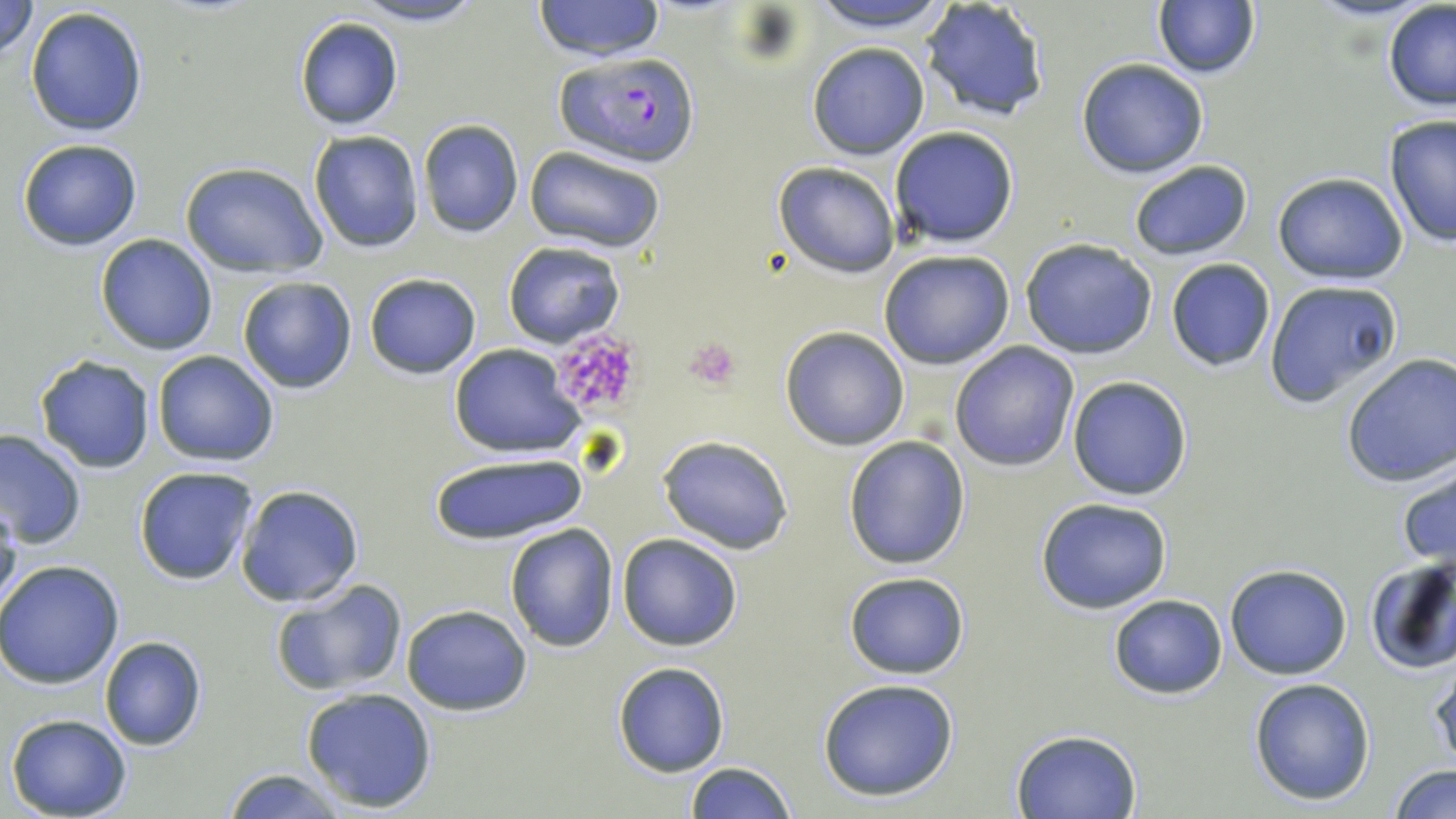

Approximate bounding boxes as [x1, y1, x2, y2] in pixels. Plasmodium falciparum-infected red blood cell locations: [557, 50, 698, 168]. Uninfected red blood cell locations: [0, 0, 38, 61], [351, 0, 489, 27], [532, 0, 663, 61], [805, 0, 953, 34], [1301, 0, 1438, 22], [920, 1, 1050, 123], [1151, 1, 1261, 81], [1382, 4, 1456, 112], [26, 5, 149, 138], [292, 17, 405, 131], [807, 41, 931, 159], [1075, 58, 1209, 178], [1383, 114, 1455, 248], [417, 119, 524, 237], [889, 126, 1020, 248], [308, 130, 424, 253], [16, 137, 144, 251], [525, 147, 667, 255], [1127, 159, 1252, 262], [178, 161, 329, 278], [772, 161, 902, 277], [1271, 171, 1409, 285], [95, 234, 217, 355], [1019, 237, 1159, 360], [503, 241, 626, 349], [879, 251, 1017, 371], [1165, 258, 1276, 372], [363, 273, 483, 379], [236, 275, 358, 394], [1263, 278, 1403, 407], [779, 327, 909, 449], [949, 341, 1080, 470], [449, 345, 588, 456], [151, 349, 279, 465], [1338, 352, 1456, 487], [34, 356, 156, 473], [1067, 375, 1193, 500], [0, 430, 87, 550], [658, 435, 795, 553], [843, 436, 971, 570], [428, 449, 590, 546], [1396, 459, 1456, 570], [134, 467, 258, 584], [236, 485, 363, 607], [1035, 497, 1173, 614], [0, 500, 23, 617], [504, 524, 618, 652], [616, 532, 744, 651], [1364, 555, 1456, 675], [0, 560, 125, 688], [1224, 565, 1352, 680], [843, 570, 971, 678], [270, 578, 409, 698], [1108, 594, 1227, 700], [401, 604, 532, 715], [99, 636, 206, 751], [1429, 660, 1456, 772], [612, 662, 730, 777], [1248, 677, 1377, 805], [817, 678, 960, 802], [299, 686, 440, 813], [5, 713, 132, 819], [1011, 728, 1141, 817], [683, 761, 795, 818], [1388, 765, 1455, 819], [221, 768, 350, 819]. Platelet locations: [549, 328, 645, 418], [685, 339, 741, 390]. Slide-level diagnosis: Plasmodium falciparum. Image is 1456×819 pixels. May-Grünwald-Giemsa-stained preparation. Thin blood film. Captured at 1000x magnification. Single field of view. Optical microscopy.